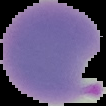
{
  "image_type": "segmented cell region with the area outside set to black",
  "image_size": "106×106 pixels",
  "preparation": "thin blood smear",
  "malaria_status": "parasitized"
}